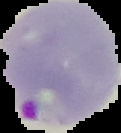
Summary:
  - Preparation: thin blood smear
  - Image type: segmented cell region with the area outside set to black
  - Malaria status: parasitized
  - Image size: 121×133 pixels